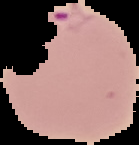

Summary:
  - Result: Plasmodium parasites identified
  - Image size: 139×145 pixels
  - Image type: segmented cell region on a black background
  - Preparation: thin blood film